Identify the parasite.
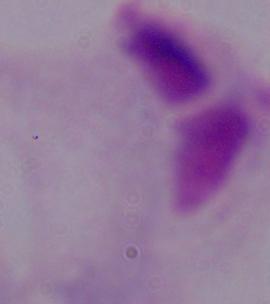

A trichomonad.

magnification = 1000x
modality = micrograph